Locate every uninfected red blood cell.
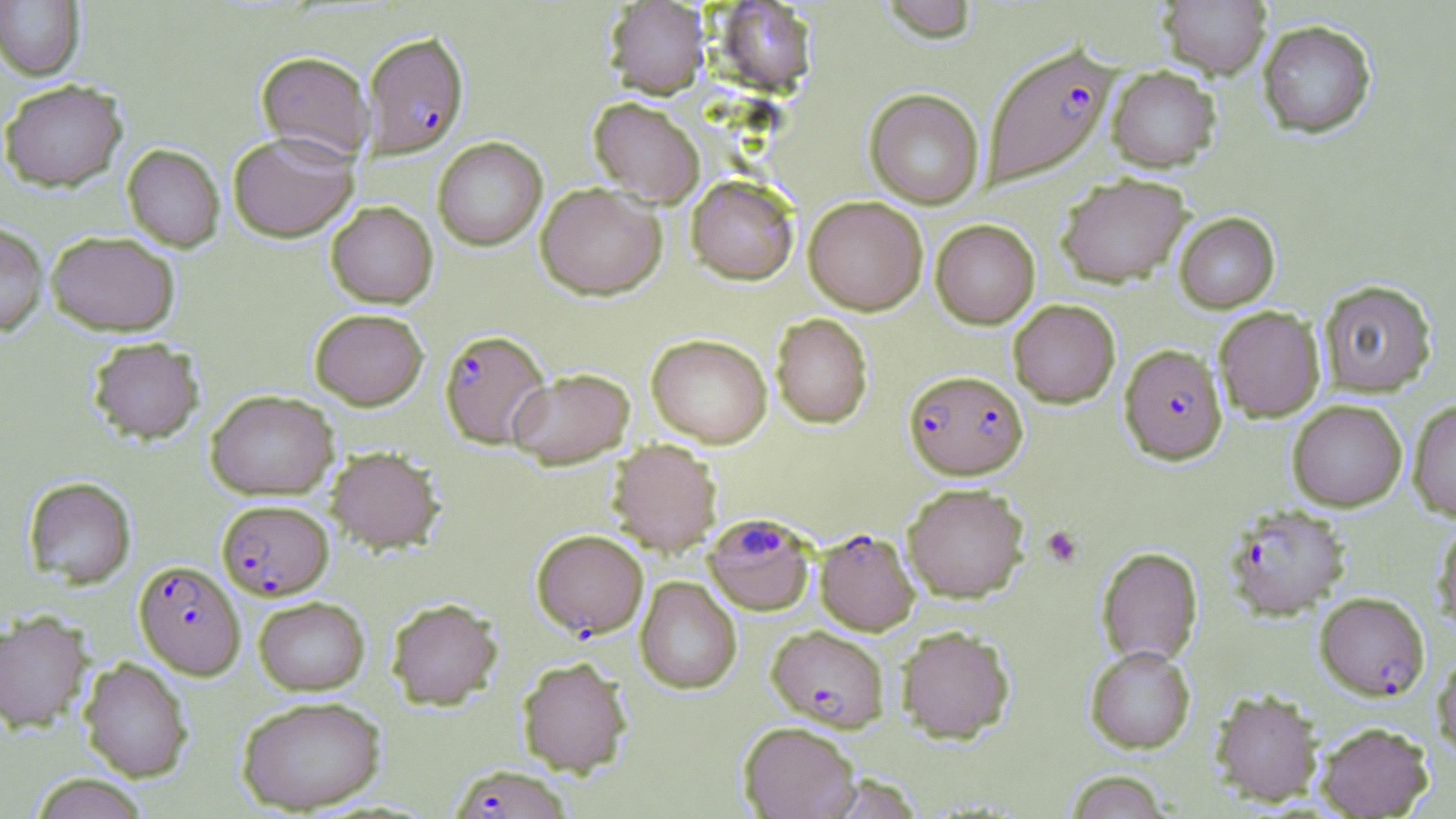

Approximate bounding boxes as [x1, y1, x2, y2] in pixels.
Uninfected red blood cells: [879, 0, 979, 43], [1158, 0, 1272, 79], [0, 1, 85, 80], [604, 1, 710, 99], [713, 1, 818, 94], [1258, 20, 1376, 138], [256, 51, 374, 161], [1107, 65, 1221, 172], [0, 79, 128, 192], [864, 89, 984, 209], [588, 97, 705, 207], [228, 130, 359, 242], [432, 137, 547, 251], [122, 143, 225, 252], [1056, 172, 1193, 287], [686, 176, 799, 285], [536, 182, 666, 300], [803, 196, 928, 315], [326, 201, 438, 308], [1173, 212, 1280, 313], [930, 219, 1040, 328], [0, 222, 48, 336], [46, 230, 180, 336], [1318, 279, 1437, 397], [1008, 299, 1120, 407], [1214, 306, 1325, 421], [310, 308, 428, 410], [771, 314, 873, 428], [646, 334, 772, 448], [86, 337, 205, 444], [507, 367, 635, 469], [205, 389, 338, 499], [1407, 399, 1456, 521], [1287, 400, 1407, 511], [607, 439, 723, 557], [325, 445, 445, 553], [23, 476, 136, 588], [902, 483, 1029, 602], [1433, 519, 1456, 634], [1097, 546, 1203, 667], [636, 576, 741, 693], [253, 596, 369, 695], [386, 597, 503, 710], [0, 610, 93, 733], [896, 625, 1016, 743], [1085, 645, 1196, 754], [1432, 651, 1456, 765], [516, 656, 633, 777], [79, 657, 193, 782], [1210, 688, 1323, 806], [236, 695, 388, 814], [739, 721, 861, 819], [1315, 722, 1434, 817], [1064, 770, 1173, 819], [29, 773, 151, 819].

Platelet locations: [1042, 525, 1083, 568]. Plasmodium falciparum-infected red blood cell locations: [362, 32, 469, 158], [983, 43, 1117, 187], [439, 329, 551, 449], [1120, 343, 1227, 464], [904, 370, 1027, 479], [216, 499, 334, 600], [1224, 503, 1351, 619], [703, 514, 815, 616], [816, 527, 919, 635], [532, 529, 648, 638], [134, 560, 245, 679], [1315, 591, 1429, 701], [766, 625, 889, 732], [449, 764, 572, 819]. Slide-level diagnosis: Plasmodium falciparum. One field of a larger specimen. May-Grünwald-Giemsa stain. Optical microscopy. 1000x magnification. Image is 1456×819 pixels. Thin blood film.